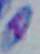
Summary:
  - Magnification: 1000x
  - Identification: Toxoplasma gondii
  - Modality: micrograph